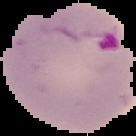 Malaria status: parasitized. From a thin blood smear. Image is 136×136 pixels. Cell region segmented out of the field of view; the surrounding area is masked to black.